Locate every malaria parasite by life-cycle stage, and every leukocyte.
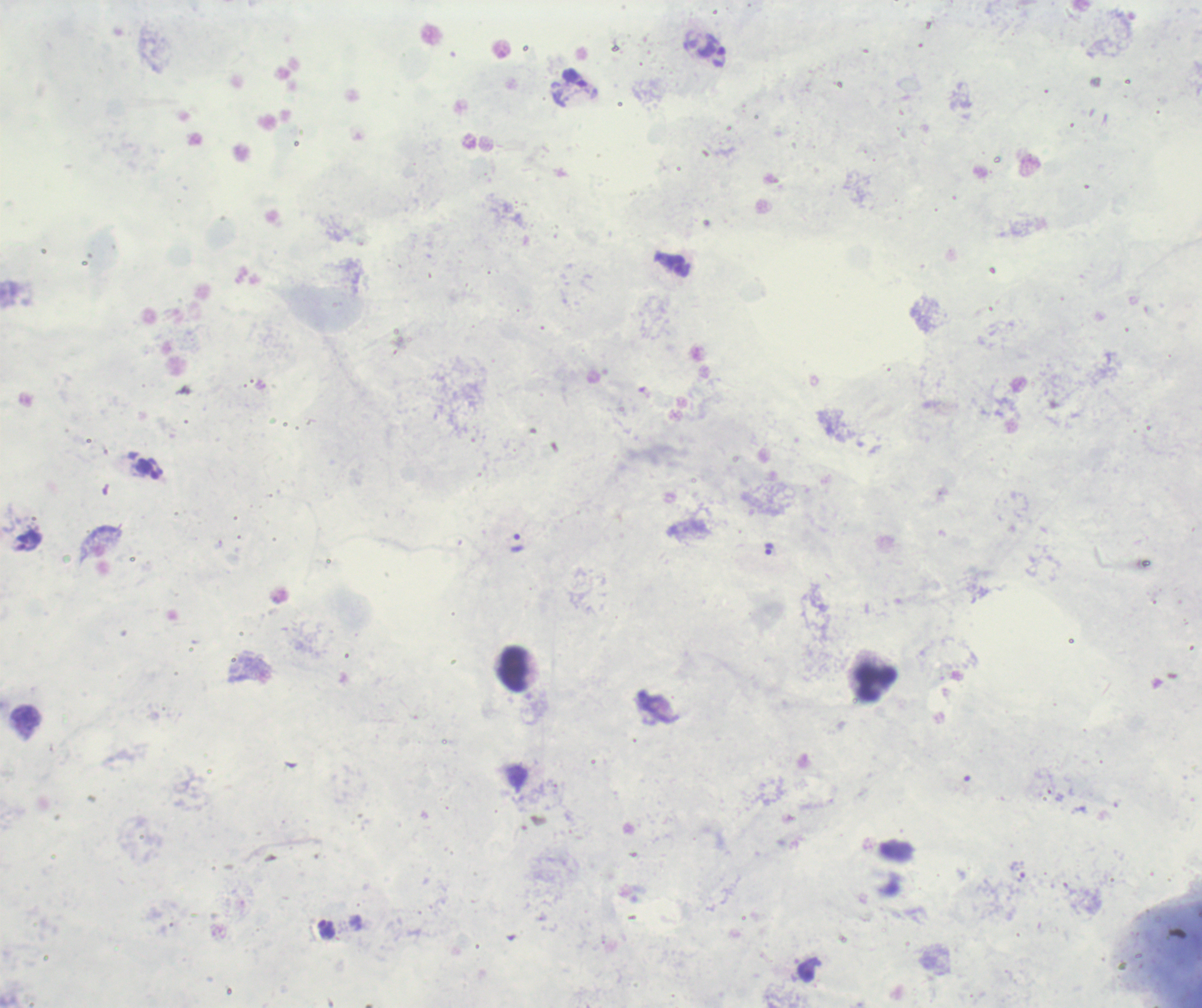
Approximate centers as {x, y} in pixels.
Trophozoites: {516, 542}, {769, 549}.
No schizont or gametocyte forms observed.
Leukocytes: {513, 669}, {876, 682}.

preparation: thick blood smear
image_size: 1202×1008 pixels
field_of_view: one from this slide
background_quality: unsatisfactory
context: previously used in a real diagnosis
magnification: 100x
stain: Romanowsky